State which cell type is depicted.
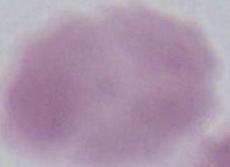
An erythrocyte.

Summary:
  - Magnification: 1000x
  - Modality: photomicrograph